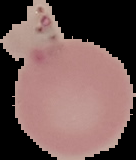
From a thin blood smear. Image is 136×160 pixels. Segmented cell region on a black background. Result: no Plasmodium parasites seen.